Outline each Plasmodium vivax-infected red blood cell.
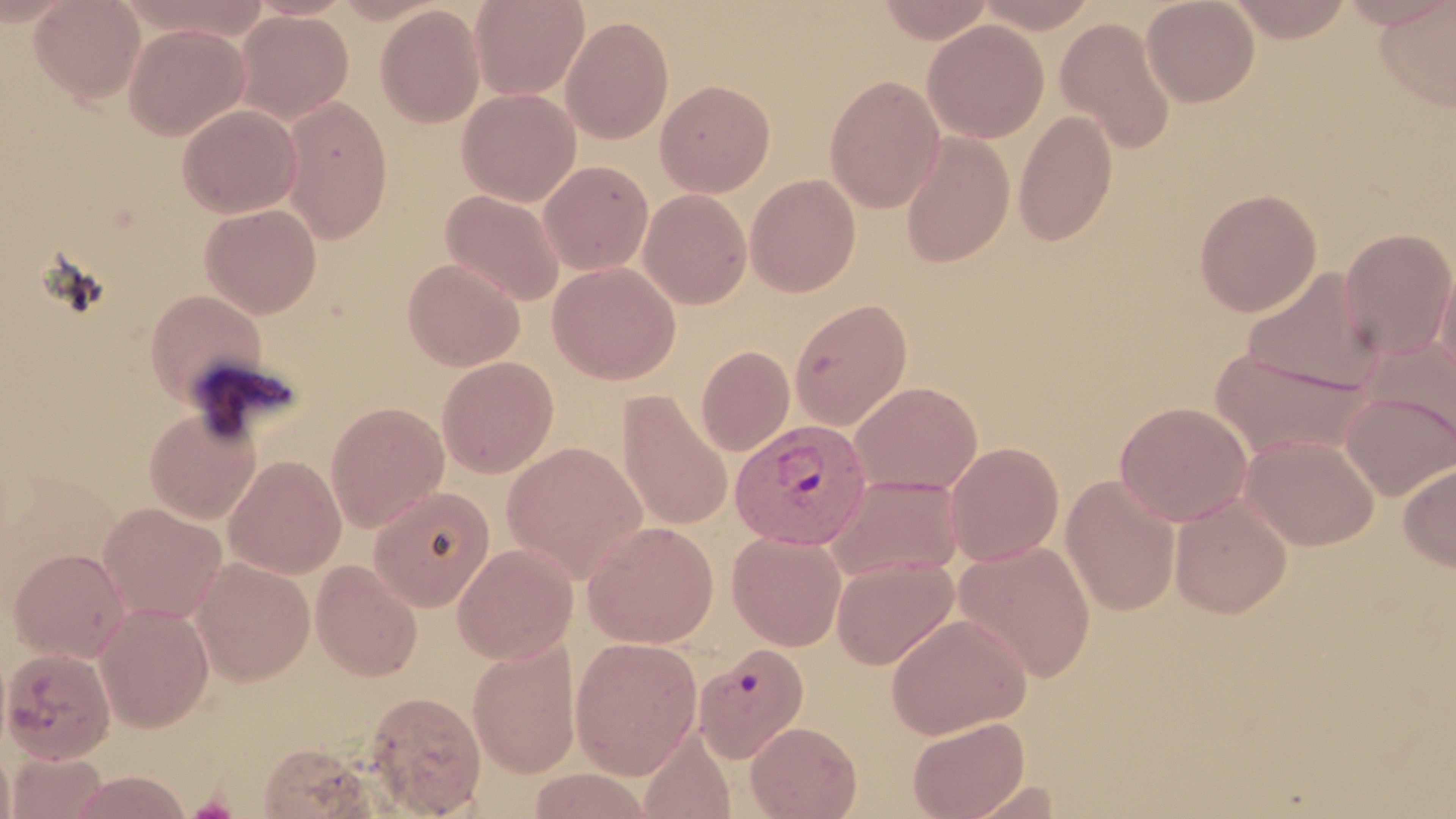
Approximate bounding boxes as [x1, y1, x2, y2] in pixels.
Plasmodium vivax-infected red blood cells: [730, 419, 875, 548].

Uninfected red blood cell locations: [29, 0, 145, 105], [470, 0, 590, 100], [875, 0, 994, 44], [973, 0, 1101, 32], [1141, 0, 1259, 108], [1225, 0, 1354, 42], [1375, 0, 1456, 113], [375, 4, 486, 128], [234, 10, 353, 124], [561, 15, 675, 145], [1056, 16, 1176, 154], [922, 19, 1048, 144], [123, 23, 249, 141], [824, 75, 945, 213], [655, 79, 775, 197], [457, 88, 581, 206], [280, 96, 392, 243], [177, 104, 302, 218], [1014, 110, 1118, 246], [900, 132, 1015, 268], [539, 160, 653, 275], [745, 174, 861, 297], [1193, 188, 1322, 316], [440, 189, 565, 306], [638, 189, 752, 309], [199, 203, 321, 318], [1339, 228, 1456, 361], [402, 259, 525, 371], [1435, 259, 1456, 389], [548, 261, 681, 385], [1242, 267, 1383, 394], [144, 289, 269, 407], [789, 298, 913, 430], [1361, 336, 1456, 456], [696, 346, 795, 456], [1210, 347, 1371, 463], [437, 356, 559, 478], [850, 381, 981, 495], [618, 391, 732, 531], [1341, 392, 1455, 501], [325, 402, 450, 532], [1115, 402, 1253, 526], [144, 406, 262, 524], [1240, 435, 1378, 551], [502, 440, 649, 583], [944, 442, 1064, 566], [225, 455, 346, 578], [1399, 462, 1456, 573], [828, 474, 965, 582], [1061, 475, 1180, 616], [368, 486, 495, 612], [1170, 495, 1292, 618], [97, 502, 227, 623], [583, 520, 719, 648], [727, 531, 847, 651], [954, 540, 1096, 682], [453, 543, 578, 663], [8, 547, 131, 662], [831, 556, 959, 670], [191, 557, 314, 686], [311, 560, 423, 681], [94, 602, 215, 731], [886, 613, 1031, 739], [569, 636, 703, 780], [467, 639, 581, 779], [693, 643, 808, 761], [1, 647, 116, 763], [364, 690, 487, 816], [907, 716, 1030, 819], [745, 721, 862, 818], [638, 733, 735, 818], [257, 741, 382, 818], [0, 744, 16, 819], [6, 752, 108, 817], [68, 770, 193, 817]. Slide-level diagnosis: Plasmodium vivax. Thin blood film. One field of a larger specimen. May-Grünwald-Giemsa-stained preparation. Image is 1456×819 pixels. Optical microscopy. 1000x magnification.